Identify the parasite.
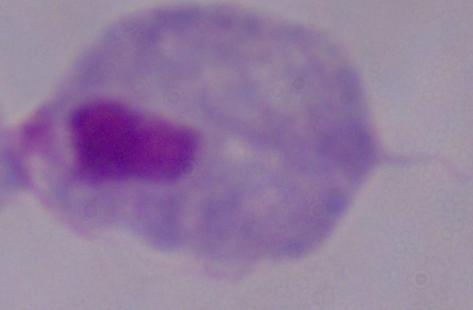
A trichomonad.

Summary:
  - Magnification: 1000x
  - Modality: micrograph